Name the parasite shown.
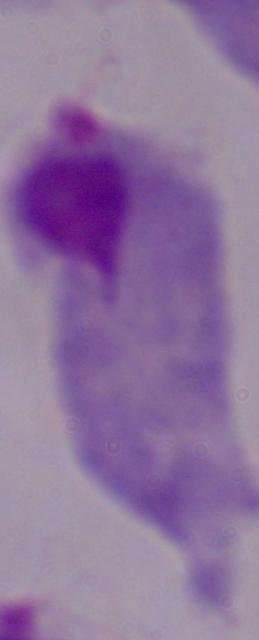
A trichomonad.

1000x magnification. Micrograph.